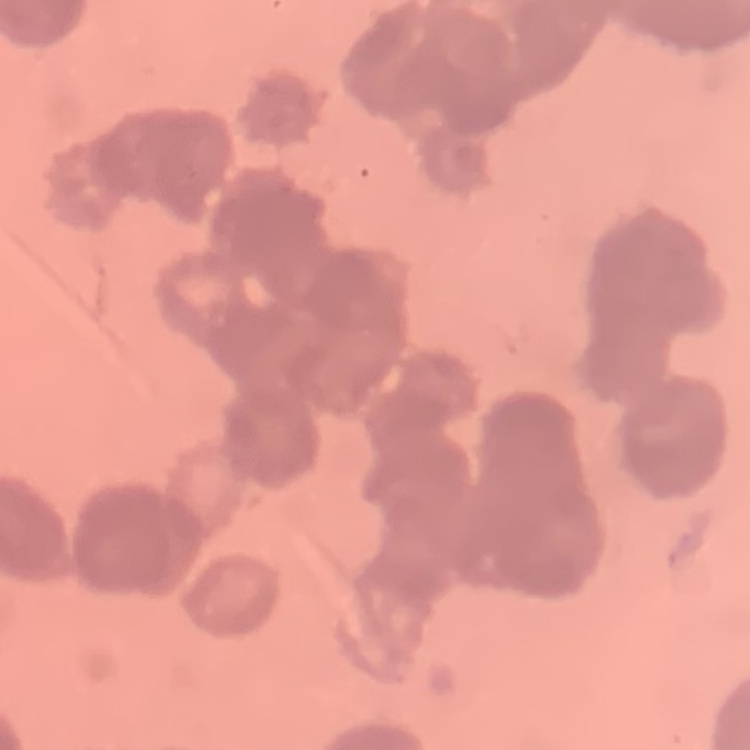

The erythrocytes show rouleaux formation. Thin blood film. Square crop of a larger photomicrograph. Stained with either Field's or Giemsa.